State which parasite is depicted.
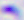

Toxoplasma gondii.

Summary:
  - Magnification: 400x
  - Modality: micrograph